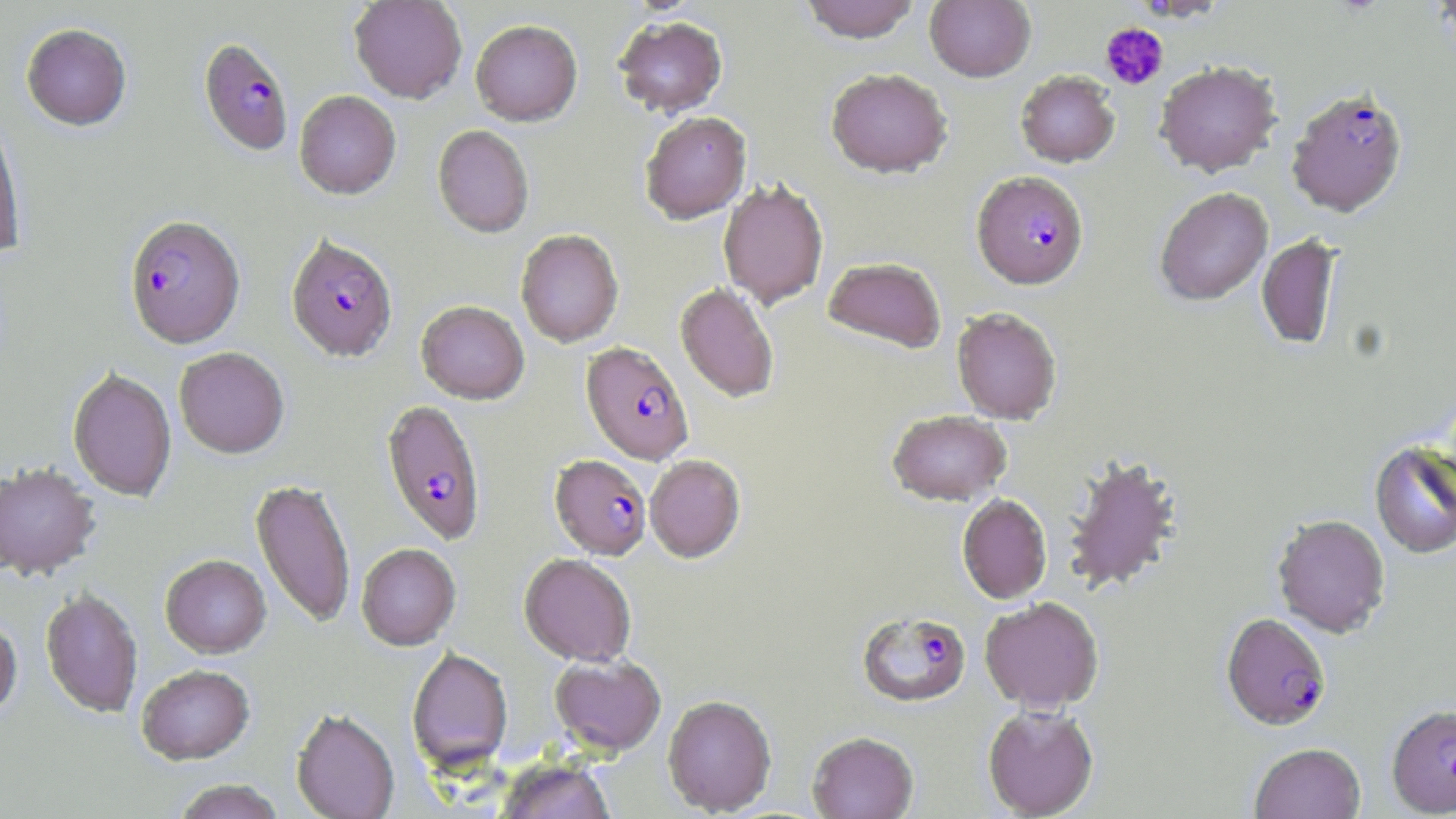

Approximate bounding boxes as (x1,y1)-(x2,y2) corner pairs in pixels. Plasmodium falciparum-infected red blood cell locations: (198,37)-(294,155), (1286,86)-(1408,217), (972,170)-(1089,289), (124,215)-(245,349), (286,235)-(398,362), (581,341)-(693,464), (381,399)-(486,545), (550,454)-(651,560), (856,611)-(971,707), (1221,612)-(1332,730), (1386,704)-(1456,816). Platelet locations: (1101,22)-(1168,89). Uninfected red blood cell locations: (349,0)-(467,103), (799,0)-(921,43), (925,0)-(1035,82), (613,16)-(728,117), (470,20)-(583,126), (21,23)-(132,130), (1154,60)-(1282,177), (825,68)-(953,178), (1015,70)-(1120,167), (294,90)-(401,198), (640,111)-(751,224), (0,112)-(26,259), (432,124)-(534,237), (718,178)-(829,309), (1154,187)-(1273,305), (515,229)-(623,347), (1256,233)-(1341,350), (823,256)-(946,353), (676,283)-(779,402), (416,300)-(529,403), (951,307)-(1062,424), (174,347)-(289,459), (67,368)-(177,502), (887,410)-(1011,506), (1369,441)-(1456,559), (1061,452)-(1183,595), (645,455)-(745,562), (0,462)-(100,581), (251,478)-(356,628), (957,494)-(1052,604), (1272,513)-(1390,637), (356,543)-(460,650), (519,553)-(636,666), (160,555)-(271,659), (41,589)-(143,718), (980,596)-(1104,711), (0,616)-(22,722), (407,647)-(512,774), (550,654)-(666,755), (137,666)-(255,766), (662,694)-(777,816), (982,705)-(1099,818), (291,708)-(400,819), (807,731)-(919,819), (1249,742)-(1366,819), (496,758)-(616,819), (172,780)-(287,819). Slide-level diagnosis: Plasmodium falciparum. Captured at 1000x magnification. Thin blood smear. Image is 1456×819 pixels. Light microscopy. May-Grünwald-Giemsa-stained preparation. Single field of view.